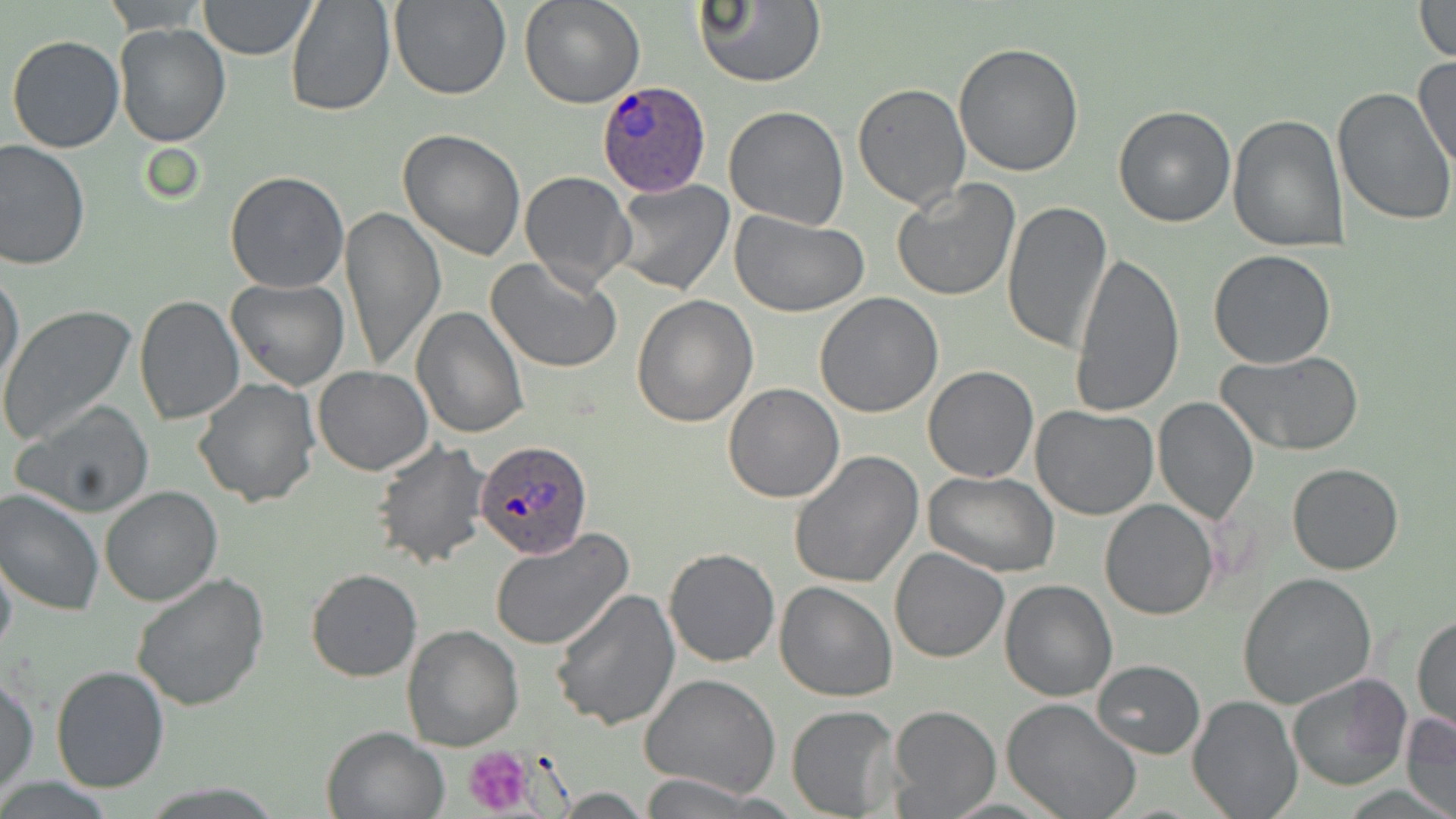
slide-level diagnosis = Plasmodium ovale
stain = May-Grünwald-Giemsa
preparation = thin blood film
platelet locations = approximate bounding boxes as [x1, y1, x2, y2] in pixels: [463, 744, 539, 816]
image size = 1456×819 pixels
modality = light microscopy
Plasmodium ovale-infected red blood cell locations = approximate bounding boxes as [x1, y1, x2, y2] in pixels: [594, 80, 713, 197], [475, 438, 592, 561]
field of view = single
magnification = 1000x
uninfected red blood cell locations = approximate bounding boxes as [x1, y1, x2, y2] in pixels: [285, 0, 396, 118], [388, 0, 510, 101], [519, 0, 645, 109], [692, 0, 824, 88], [103, 1, 210, 33], [198, 1, 317, 59], [1411, 1, 1456, 62], [114, 23, 232, 148], [6, 34, 125, 154], [953, 43, 1086, 178], [1414, 54, 1456, 173], [853, 83, 971, 211], [1332, 88, 1456, 229], [1112, 104, 1236, 228], [723, 105, 851, 229], [1228, 113, 1348, 251], [398, 129, 527, 261], [0, 139, 92, 270], [519, 171, 635, 292], [224, 172, 349, 294], [892, 178, 1021, 302], [609, 180, 736, 297], [1001, 198, 1113, 356], [339, 206, 445, 372], [729, 209, 870, 316], [1207, 249, 1337, 369], [1069, 253, 1183, 419], [488, 256, 623, 373], [0, 268, 24, 392], [225, 278, 348, 391], [814, 293, 944, 417], [631, 295, 759, 428], [133, 297, 244, 425], [410, 305, 528, 439], [0, 306, 137, 447], [1218, 351, 1365, 456], [921, 365, 1037, 483], [312, 366, 432, 476], [192, 376, 320, 507], [722, 382, 845, 503], [1153, 396, 1258, 523], [12, 401, 156, 518], [1031, 405, 1158, 520], [371, 440, 492, 569], [788, 451, 924, 589], [1288, 462, 1405, 575], [924, 472, 1062, 578], [101, 485, 222, 606], [0, 489, 104, 617], [1099, 499, 1220, 621], [490, 528, 634, 651], [663, 546, 781, 666], [889, 547, 1010, 663], [0, 549, 17, 661], [305, 569, 421, 681], [1237, 571, 1376, 710], [131, 572, 269, 711], [1000, 579, 1118, 701], [773, 582, 897, 702], [548, 588, 679, 729], [1412, 614, 1455, 737], [402, 626, 524, 750], [1092, 659, 1205, 758], [50, 665, 169, 794], [1286, 672, 1413, 792], [1, 674, 39, 794], [640, 674, 780, 798], [1189, 695, 1301, 818], [1000, 697, 1143, 819], [787, 705, 900, 817], [886, 705, 1001, 817], [1401, 712, 1456, 819], [320, 726, 448, 819], [636, 774, 772, 817]